Identify the blood parasite species.
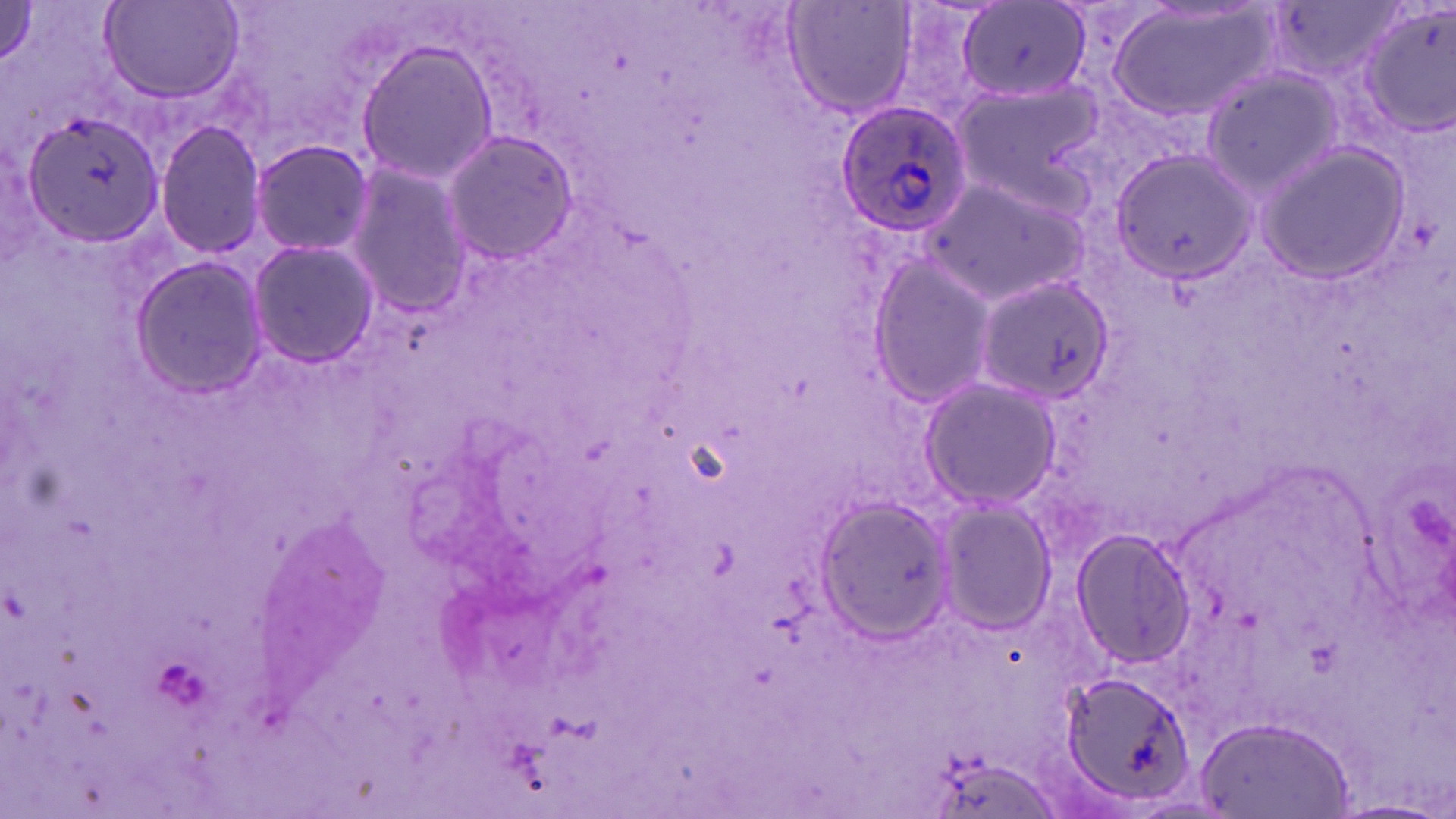
Plasmodium ovale.

Approximate bounding boxes as named x1/y1/x2/y2 corners in pixels. Uninfected red blood cell locations: (x1=784, y1=0, x2=917, y2=118), (x1=1108, y1=1, x2=1281, y2=124), (x1=1358, y1=1, x2=1456, y2=139), (x1=100, y1=2, x2=244, y2=103), (x1=959, y1=3, x2=1090, y2=102), (x1=354, y1=38, x2=501, y2=186), (x1=1200, y1=67, x2=1343, y2=197), (x1=955, y1=80, x2=1107, y2=202), (x1=16, y1=103, x2=167, y2=250), (x1=155, y1=121, x2=265, y2=259), (x1=440, y1=129, x2=581, y2=266), (x1=250, y1=139, x2=374, y2=258), (x1=1255, y1=141, x2=1412, y2=285), (x1=1106, y1=146, x2=1252, y2=289), (x1=342, y1=161, x2=470, y2=314), (x1=920, y1=171, x2=1091, y2=306), (x1=248, y1=239, x2=377, y2=368), (x1=869, y1=254, x2=996, y2=408), (x1=130, y1=257, x2=269, y2=398), (x1=977, y1=275, x2=1117, y2=405), (x1=919, y1=376, x2=1062, y2=510), (x1=814, y1=495, x2=955, y2=638), (x1=935, y1=500, x2=1055, y2=632), (x1=1073, y1=528, x2=1196, y2=665), (x1=1061, y1=669, x2=1201, y2=807), (x1=1200, y1=717, x2=1354, y2=819). Plasmodium ovale-infected red blood cell locations: (x1=832, y1=99, x2=974, y2=238). 1000x magnification. May-Grünwald-Giemsa stain. One field of a larger specimen. Light microscopy. Thin blood film. Image is 1456×819 pixels.